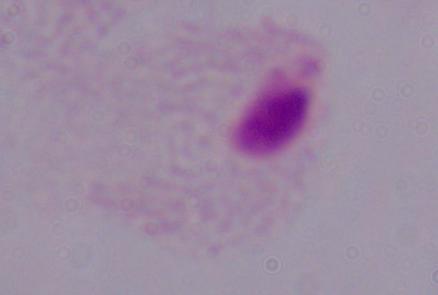
{
  "magnification": "1000x",
  "identification": "trichomonad",
  "modality": "photomicrograph"
}